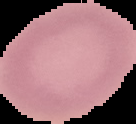
From a thin blood film. Image is 136×124 pixels. The area outside the segmented cell region is set to black. Malaria status: uninfected.